Classify this cell by malaria status.
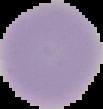

Uninfected.

Cell region segmented out of the field of view; the surrounding area is masked to black. From a thin blood film. Image is 103×109 pixels.